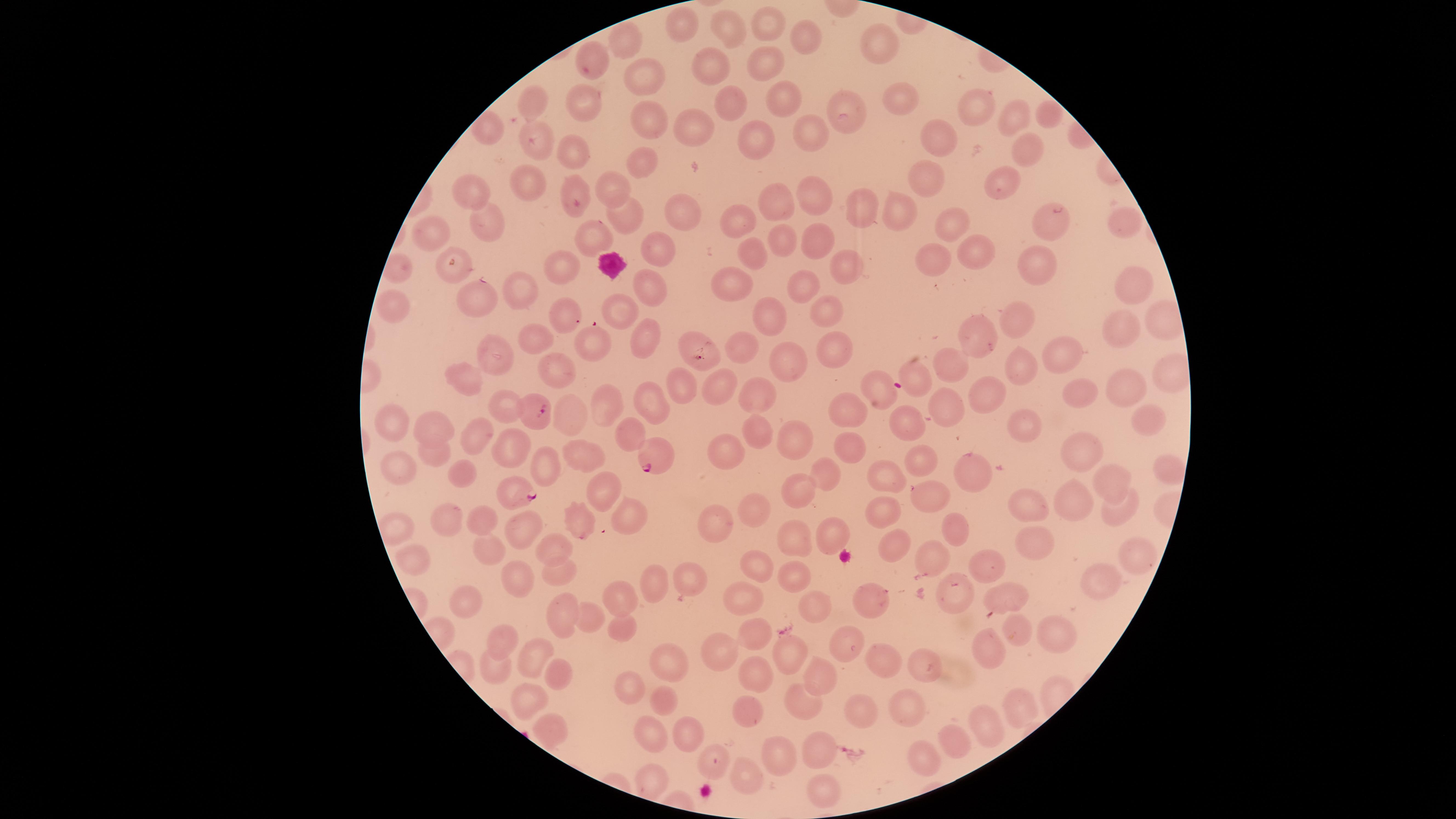
Approximate marker points as (x, y) in pixels.
Summary:
  - Uninfected RBCs: (766, 23), (678, 28), (728, 28), (804, 33), (876, 42), (622, 47), (596, 62), (713, 63), (762, 64), (647, 74), (902, 96), (588, 97), (780, 98), (730, 101), (982, 104), (532, 107), (647, 113), (842, 113), (1049, 114), (1015, 120), (695, 129), (809, 133), (532, 136), (756, 139), (944, 141), (1030, 151), (578, 152), (646, 163), (519, 175), (1006, 177), (928, 178), (576, 186), (607, 188), (480, 191), (814, 195), (778, 203), (677, 206), (899, 207), (862, 209), (740, 216), (1043, 218), (1122, 218), (950, 219), (626, 221), (482, 229), (438, 234), (779, 236), (591, 239), (816, 243), (972, 248), (656, 252), (936, 254), (756, 257), (451, 265), (1039, 267), (559, 269), (844, 269), (730, 278), (1130, 280), (517, 285), (806, 287), (652, 288), (477, 301), (825, 308), (562, 312), (616, 315), (769, 315), (1019, 319), (987, 328), (1113, 329), (647, 336), (533, 337), (596, 344), (693, 344), (743, 344), (832, 346), (499, 353), (1065, 353), (780, 360), (957, 361), (557, 365), (1024, 366), (916, 372), (458, 376), (716, 382), (881, 384), (678, 387), (987, 389), (1123, 389), (1078, 391), (755, 396), (653, 400), (607, 402), (946, 403), (503, 404), (846, 406), (576, 418), (908, 419), (1144, 420), (1024, 424), (396, 426), (435, 426), (757, 436), (471, 439), (791, 441), (509, 443), (622, 443), (849, 447), (1079, 451), (720, 453), (435, 454), (579, 459), (919, 460), (397, 464), (551, 467), (464, 472), (968, 474), (823, 477), (885, 479), (1113, 483), (595, 493), (796, 496), (931, 500), (1078, 503), (755, 509), (1119, 510), (1026, 511), (882, 513), (449, 516), (482, 518), (579, 519), (628, 519), (715, 527), (951, 529), (524, 532), (826, 538), (794, 542), (487, 544), (555, 546), (1033, 548), (887, 549), (983, 557), (1136, 559), (413, 561), (929, 563), (754, 567), (557, 568), (795, 573), (521, 577), (654, 581), (687, 581), (1108, 586), (954, 594), (1010, 596), (472, 597), (746, 597), (621, 598), (869, 600), (812, 603), (558, 613), (585, 616), (620, 626), (1017, 630), (755, 632), (1051, 632), (500, 637), (843, 642), (986, 648), (531, 649), (718, 654), (791, 656), (664, 660), (882, 662), (924, 663), (494, 667), (819, 675), (757, 676), (559, 677), (628, 691), (527, 700), (664, 700), (798, 701), (1018, 707), (751, 710), (853, 712), (907, 712), (552, 726), (648, 726), (984, 729), (687, 732), (953, 739), (821, 748), (779, 754), (921, 754), (711, 762), (653, 775), (746, 779), (824, 789)
  - Parasitized RBCs: (532, 411), (658, 458), (520, 493)
  - WBCs: (613, 265)
  - Preparation: thin smear of blood
  - Stain: Giemsa
  - Visible region: circular
  - Presence: malaria parasites detected
  - Image size: 1456×819 pixels
  - Field of view: single
  - Capture: smartphone photograph through the microscope eyepiece
  - Species: Plasmodium falciparum